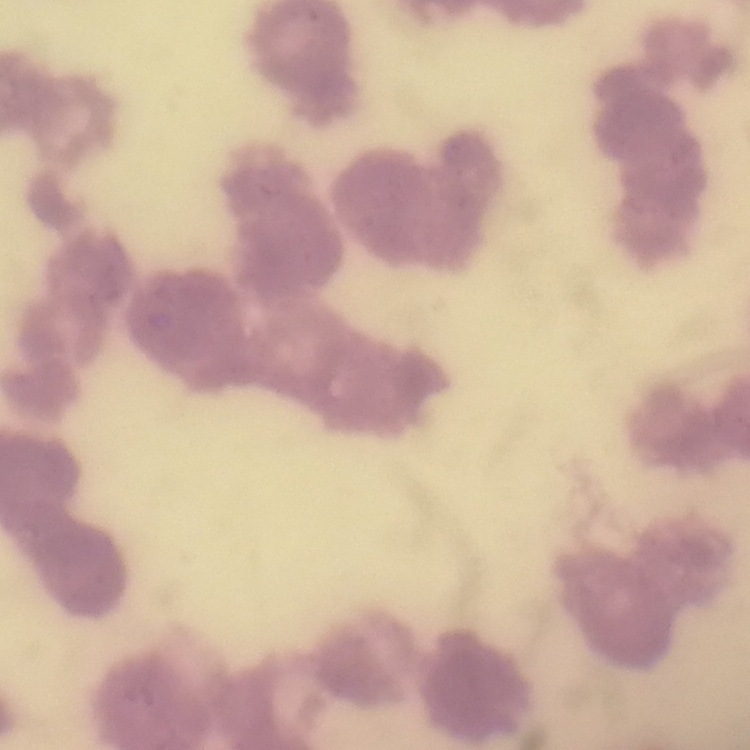
The erythrocytes show rouleaux formation. Thin blood smear. Square crop of a larger photomicrograph. Stained with either Field's or Giemsa.